Give a bounding box for every artifact (stain precipitate or debris).
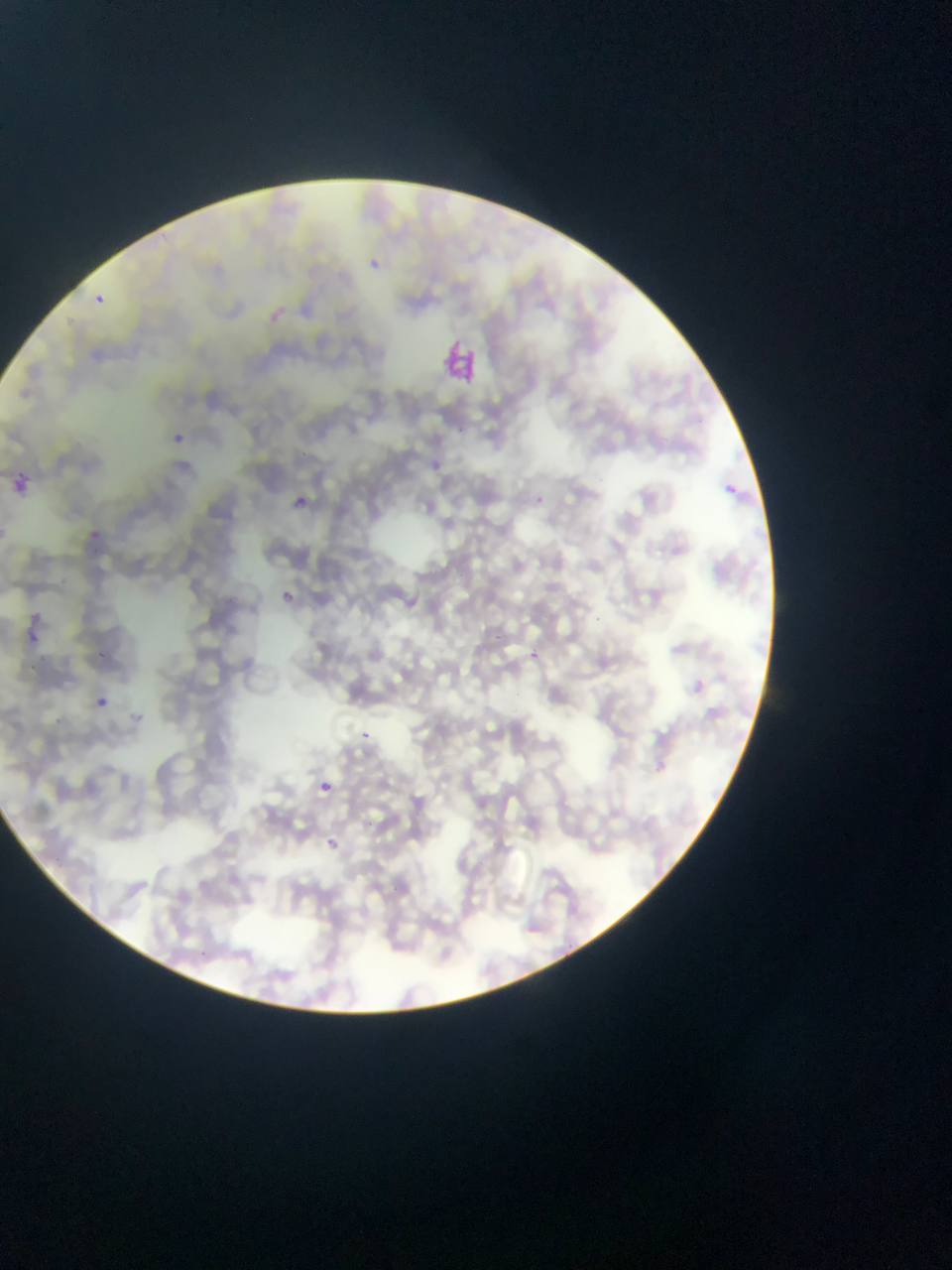
Approximate bounding boxes as [left, top, right, bottom] in pixels.
Artifacts (stain precipitate or debris): [442, 337, 482, 384].

preparation: thin blood smear
capture: mobile-phone photograph through a microscope
plasmodium_parasite_locations: 'approximate bounding boxes as [left, top, right, bottom] in pixels: [361, 259, 381, 272], [95, 290, 105, 307], [167, 425, 187, 452], [427, 454, 440, 472], [10, 472, 29, 493], [721, 477, 737, 493], [292, 492, 317, 521], [529, 494, 549, 506], [90, 529, 101, 539], [280, 587, 302, 612], [31, 610, 40, 620], [29, 633, 38, 643], [92, 649, 105, 656], [528, 652, 545, 664], [96, 696, 108, 707], [361, 730, 371, 739], [318, 779, 330, 791], [326, 837, 340, 850]'
field_of_view: single
country: Ghana
image_size: 952×1270 pixels